Locate platelets.
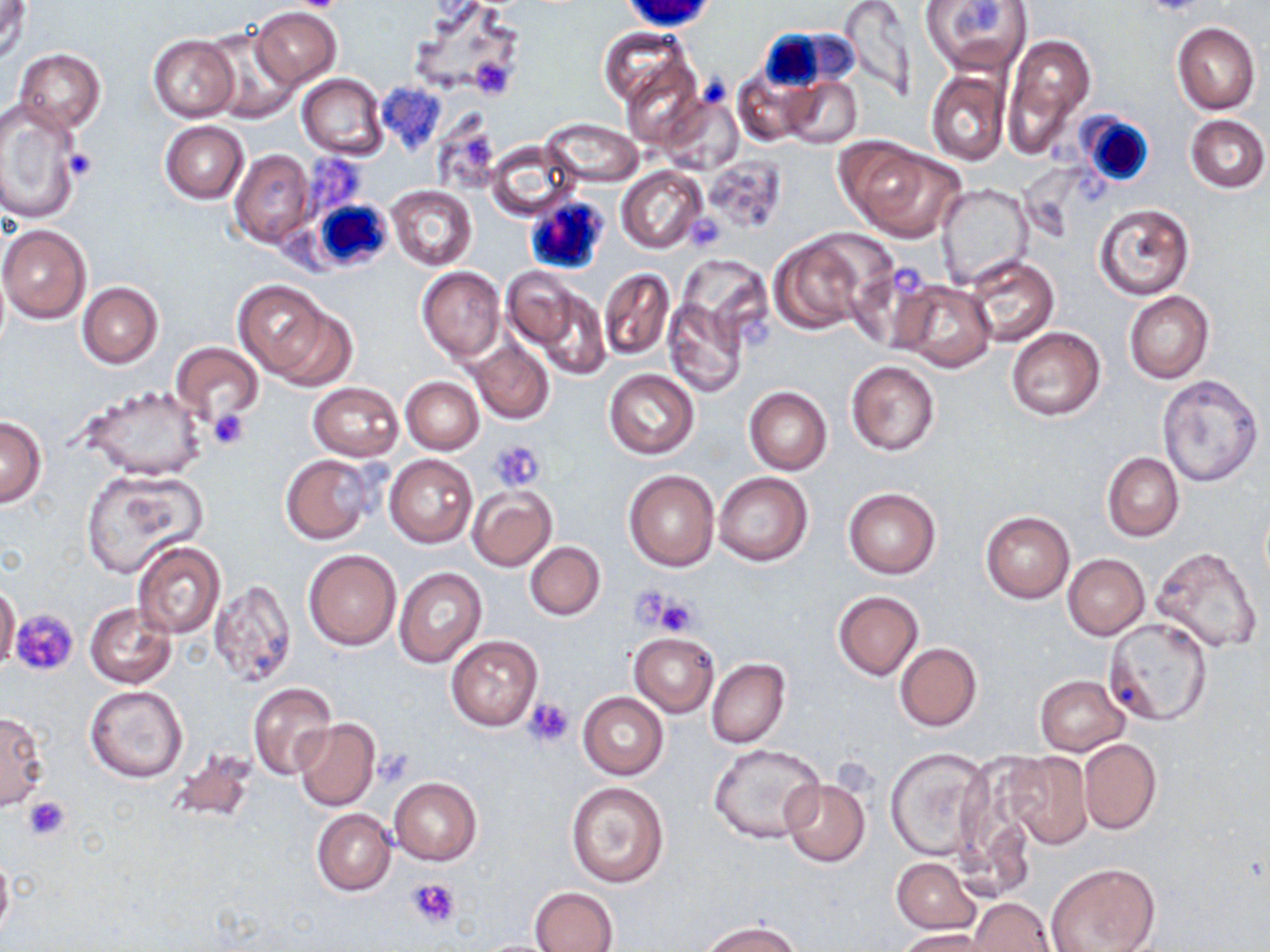
Approximate bounding boxes as (x1,y1)-(x2,y2) corner pairs in pixels.
Platelets: (293,0)-(343,12), (470,56)-(517,99), (63,148)-(99,182), (683,213)-(724,250), (889,262)-(921,294), (743,322)-(772,346), (209,408)-(249,450), (491,442)-(545,491), (628,583)-(678,632), (654,595)-(699,636), (11,609)-(79,677), (522,697)-(574,748), (372,751)-(414,787), (21,794)-(71,841), (406,877)-(460,928).

White blood cell locations: (756,27)-(836,96), (1060,111)-(1155,191), (523,194)-(609,276), (310,196)-(393,275). Uninfected red blood cell locations: (1,0)-(31,63), (406,0)-(529,99), (836,0)-(918,99), (919,0)-(1032,76), (251,6)-(341,89), (1171,22)-(1261,114), (201,28)-(301,123), (597,29)-(689,110), (1002,32)-(1096,158), (148,35)-(239,120), (13,49)-(106,134), (620,59)-(705,150), (732,65)-(816,147), (926,69)-(1010,166), (297,74)-(387,159), (781,76)-(862,149), (660,94)-(742,177), (0,101)-(83,225), (1185,115)-(1269,193), (541,118)-(643,187), (160,121)-(248,203), (486,140)-(582,219), (841,140)-(964,240), (230,148)-(316,248), (701,156)-(786,233), (617,166)-(707,254), (935,184)-(1033,287), (388,185)-(476,270), (1094,203)-(1194,300), (683,212)-(727,253), (0,224)-(91,323), (769,236)-(870,335), (964,254)-(1059,347), (850,260)-(939,352), (418,267)-(505,362), (503,267)-(588,362), (599,268)-(674,360), (894,279)-(996,373), (234,280)-(345,383), (76,281)-(163,368), (532,288)-(610,381), (1124,292)-(1214,383), (664,298)-(748,397), (1006,327)-(1105,420), (471,338)-(553,424), (169,342)-(265,427), (845,360)-(940,455), (604,369)-(698,458), (1158,374)-(1263,487), (401,377)-(483,455), (308,381)-(404,461), (80,385)-(207,482), (744,386)-(832,475), (0,416)-(47,506), (1102,452)-(1184,541), (280,454)-(376,545), (386,454)-(477,548), (623,468)-(719,572), (81,471)-(206,578), (714,472)-(813,566), (467,485)-(557,570), (845,489)-(939,579), (979,510)-(1074,604), (131,542)-(226,640), (525,542)-(606,620), (1151,546)-(1263,654), (303,549)-(401,650), (1062,554)-(1149,640), (394,567)-(486,669), (209,579)-(296,687), (0,584)-(20,671), (833,591)-(923,679), (85,602)-(176,689), (1103,617)-(1213,727), (628,631)-(719,717), (447,635)-(541,730), (894,642)-(982,731), (707,658)-(790,747), (1035,675)-(1129,755), (248,682)-(337,781), (86,686)-(188,783), (578,692)-(668,780), (0,708)-(48,811), (294,718)-(380,812), (1079,739)-(1160,834), (708,744)-(825,844), (885,748)-(992,861), (164,749)-(259,826), (1000,751)-(1093,848), (389,777)-(482,865), (780,778)-(871,867), (564,780)-(669,888), (311,809)-(396,895), (0,852)-(14,942), (892,857)-(980,934), (1045,862)-(1161,952), (530,887)-(616,952), (970,897)-(1055,952), (700,921)-(805,952), (897,929)-(994,952). Slide-level diagnosis: negative for blood parasites. 1000x magnification. Thin blood smear. Optical microscopy. May-Grünwald-Giemsa stain. Image is 1270×952 pixels. One field of a larger specimen.